Outline each blood parasite and name the species.
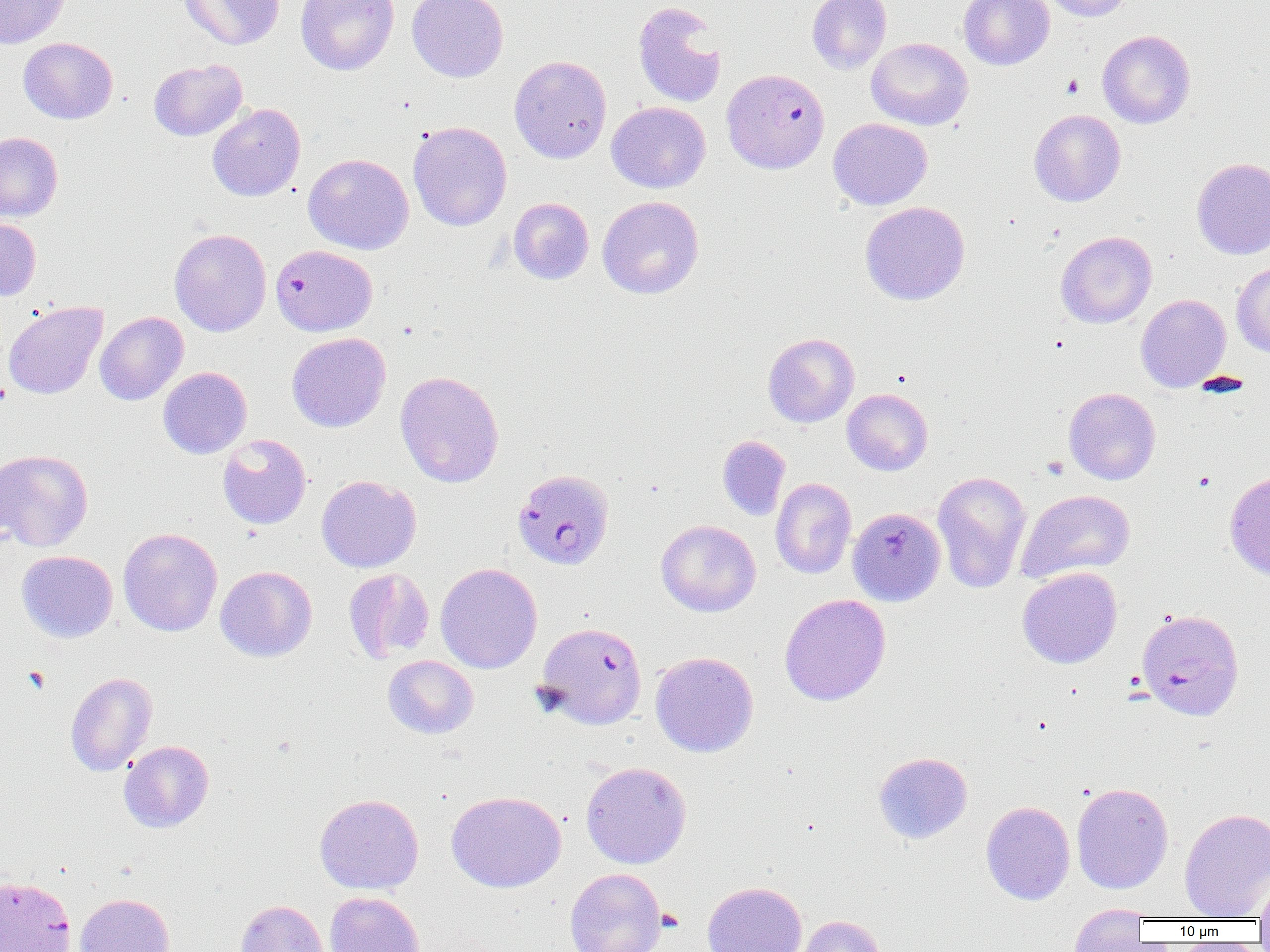
Approximate bounding boxes as [x1, y1, x2, y2] in pixels.
Plasmodium falciparum-infected red blood cells: [721, 68, 830, 173], [271, 245, 377, 336], [512, 468, 615, 570], [1136, 608, 1245, 721], [535, 621, 647, 729].
No Plasmodium ovale, Plasmodium malariae, Plasmodium vivax, Babesia divergens, or Trypanosoma brucei observed.

Summary:
  - Uninfected red blood cell locations: [178, 0, 285, 50], [296, 0, 399, 75], [407, 0, 508, 82], [806, 0, 892, 74], [959, 0, 1053, 70], [1039, 0, 1135, 21], [0, 1, 70, 49], [633, 1, 727, 107], [1097, 30, 1195, 128], [18, 37, 118, 124], [866, 37, 972, 130], [509, 55, 612, 164], [148, 58, 248, 141], [607, 101, 710, 193], [207, 103, 305, 201], [1029, 109, 1126, 206], [828, 118, 932, 210], [407, 121, 512, 231], [0, 132, 63, 221], [303, 153, 414, 254], [1191, 158, 1270, 259], [597, 196, 704, 299], [508, 197, 594, 285], [860, 201, 970, 305], [0, 217, 41, 301], [169, 228, 272, 337], [1055, 231, 1157, 328], [1232, 261, 1270, 358], [1135, 294, 1232, 392], [3, 301, 107, 399], [95, 311, 188, 405], [286, 332, 391, 432], [763, 333, 859, 427], [158, 367, 252, 459], [395, 371, 504, 488], [1063, 387, 1161, 485], [842, 389, 933, 475], [217, 434, 311, 529], [717, 435, 790, 521], [0, 448, 93, 552], [932, 470, 1032, 593], [1224, 470, 1270, 579], [316, 475, 421, 573], [770, 477, 856, 579], [1016, 489, 1136, 583], [847, 507, 946, 606], [656, 519, 761, 617], [118, 527, 223, 637], [16, 550, 118, 643], [435, 563, 543, 674], [215, 565, 317, 662], [1017, 567, 1122, 669], [343, 568, 435, 664], [779, 594, 891, 706], [650, 651, 759, 757], [383, 655, 479, 739], [65, 672, 157, 776], [118, 740, 214, 833], [873, 752, 972, 844], [581, 761, 692, 869], [1071, 782, 1174, 894], [446, 791, 567, 892], [314, 793, 423, 894], [981, 801, 1075, 905], [1179, 807, 1270, 919], [565, 867, 666, 951], [1255, 871, 1270, 924], [0, 876, 76, 952], [702, 881, 807, 952], [324, 891, 425, 952], [75, 893, 175, 952], [235, 900, 330, 952], [1068, 905, 1150, 950], [792, 914, 886, 952]
  - Platelet locations: [1061, 74, 1084, 99], [1041, 455, 1069, 480], [656, 908, 684, 932]
  - Slide-level diagnosis: Plasmodium falciparum
  - Magnification: 1000x
  - Field of view: single
  - Preparation: thin blood film
  - Image size: 1270×952 pixels
  - Modality: optical microscopy